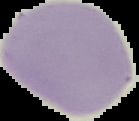

preparation: thin blood smear
malaria_status: uninfected
image_type: segmented cell region with the area outside set to black
image_size: 139×121 pixels